Locate every Plasmodium parasite.
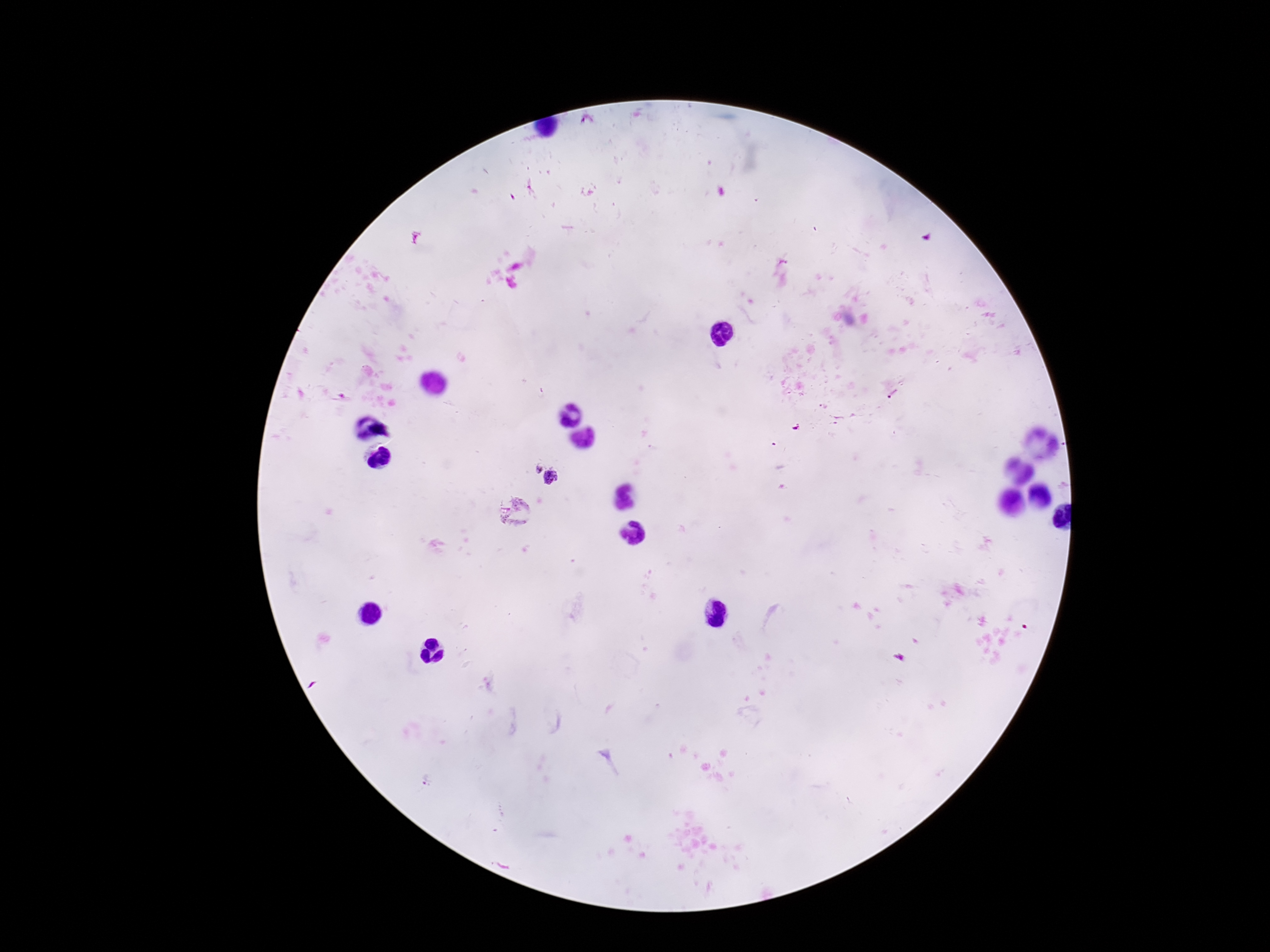

Approximate centers as (x, y) in pixels.
Plasmodium parasites: (893, 394), (534, 466), (552, 479), (516, 513).

preparation: thick peripheral-blood smear
image_size: 1270×952 pixels
patient_malaria_status: positive
magnification: 100x
stain: Giemsa
field_of_view: one from this slide
capture: smartphone camera through the microscope eyepiece